State which parasite is depicted.
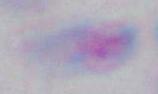

Toxoplasma gondii.

1000x magnification. Photomicrograph.